Report the malaria status of this cell.
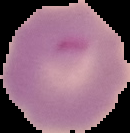
Parasitized.

Summary:
  - Image type: cell region segmented out of the field of view; surrounding area masked to black
  - Preparation: thin blood smear
  - Image size: 130×133 pixels